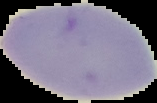
Summary:
  - Image size: 157×103 pixels
  - Preparation: thin blood smear
  - Result: no malaria parasites detected
  - Image type: segmented cell region with the area outside set to black